Locate every uninfected red blood cell.
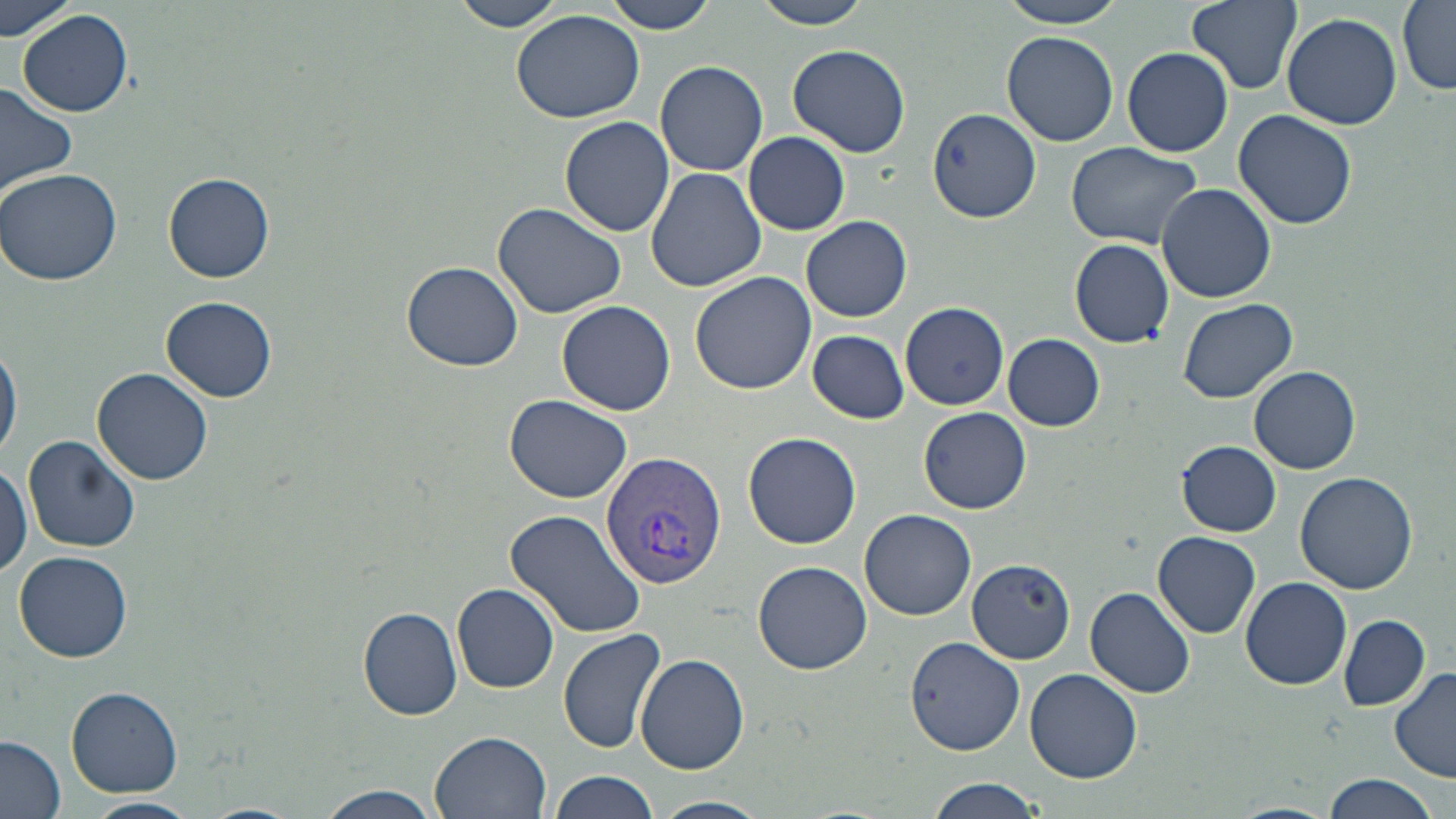
Approximate bounding boxes as named x1/y1/x2/y2 corners in pixels.
Uninfected red blood cells: (x1=0, y1=0, x2=79, y2=42), (x1=447, y1=0, x2=570, y2=33), (x1=605, y1=0, x2=721, y2=33), (x1=754, y1=0, x2=876, y2=27), (x1=993, y1=0, x2=1136, y2=29), (x1=1187, y1=0, x2=1301, y2=93), (x1=1398, y1=2, x2=1456, y2=92), (x1=16, y1=9, x2=133, y2=116), (x1=510, y1=9, x2=646, y2=124), (x1=1281, y1=12, x2=1402, y2=130), (x1=1001, y1=31, x2=1120, y2=147), (x1=786, y1=43, x2=912, y2=158), (x1=1122, y1=48, x2=1233, y2=156), (x1=656, y1=61, x2=768, y2=176), (x1=0, y1=83, x2=78, y2=200), (x1=928, y1=109, x2=1042, y2=222), (x1=1234, y1=109, x2=1357, y2=229), (x1=560, y1=116, x2=675, y2=239), (x1=743, y1=131, x2=848, y2=235), (x1=1065, y1=138, x2=1207, y2=251), (x1=645, y1=167, x2=766, y2=292), (x1=0, y1=168, x2=125, y2=286), (x1=162, y1=174, x2=276, y2=283), (x1=1157, y1=183, x2=1276, y2=303), (x1=492, y1=202, x2=626, y2=318), (x1=802, y1=214, x2=912, y2=323), (x1=1069, y1=238, x2=1174, y2=348), (x1=401, y1=259, x2=526, y2=371), (x1=689, y1=269, x2=818, y2=394), (x1=160, y1=294, x2=277, y2=403), (x1=1176, y1=295, x2=1297, y2=404), (x1=556, y1=300, x2=676, y2=417), (x1=899, y1=300, x2=1010, y2=410), (x1=807, y1=330, x2=909, y2=423), (x1=1003, y1=334, x2=1105, y2=430), (x1=0, y1=339, x2=21, y2=463), (x1=1250, y1=364, x2=1362, y2=474), (x1=93, y1=367, x2=215, y2=487), (x1=505, y1=394, x2=633, y2=503), (x1=919, y1=406, x2=1030, y2=513), (x1=742, y1=430, x2=862, y2=550), (x1=22, y1=436, x2=141, y2=552), (x1=1175, y1=440, x2=1281, y2=536), (x1=0, y1=459, x2=32, y2=580), (x1=1296, y1=469, x2=1419, y2=594), (x1=859, y1=508, x2=976, y2=620), (x1=505, y1=509, x2=646, y2=638), (x1=1153, y1=531, x2=1261, y2=638), (x1=14, y1=549, x2=133, y2=662), (x1=754, y1=559, x2=873, y2=674), (x1=968, y1=560, x2=1079, y2=661), (x1=1241, y1=576, x2=1352, y2=690), (x1=453, y1=582, x2=559, y2=692), (x1=1085, y1=586, x2=1195, y2=698), (x1=358, y1=605, x2=463, y2=721), (x1=1338, y1=614, x2=1431, y2=711), (x1=557, y1=629, x2=665, y2=754), (x1=906, y1=635, x2=1027, y2=754), (x1=635, y1=652, x2=749, y2=774), (x1=1389, y1=667, x2=1456, y2=783), (x1=1026, y1=668, x2=1141, y2=783), (x1=67, y1=686, x2=184, y2=798), (x1=431, y1=730, x2=550, y2=818), (x1=1, y1=736, x2=68, y2=818), (x1=549, y1=770, x2=658, y2=819), (x1=1319, y1=772, x2=1444, y2=819), (x1=924, y1=778, x2=1045, y2=818), (x1=309, y1=784, x2=449, y2=819), (x1=82, y1=796, x2=197, y2=819), (x1=654, y1=797, x2=768, y2=819), (x1=1228, y1=802, x2=1340, y2=819), (x1=196, y1=803, x2=302, y2=819).

Plasmodium vivax-infected red blood cell locations: (x1=599, y1=449, x2=728, y2=587). Slide-level diagnosis: Plasmodium vivax. Single field of view. Thin blood film. Image is 1456×819 pixels. May-Grünwald-Giemsa-stained preparation. Light microscopy. 1000x magnification.